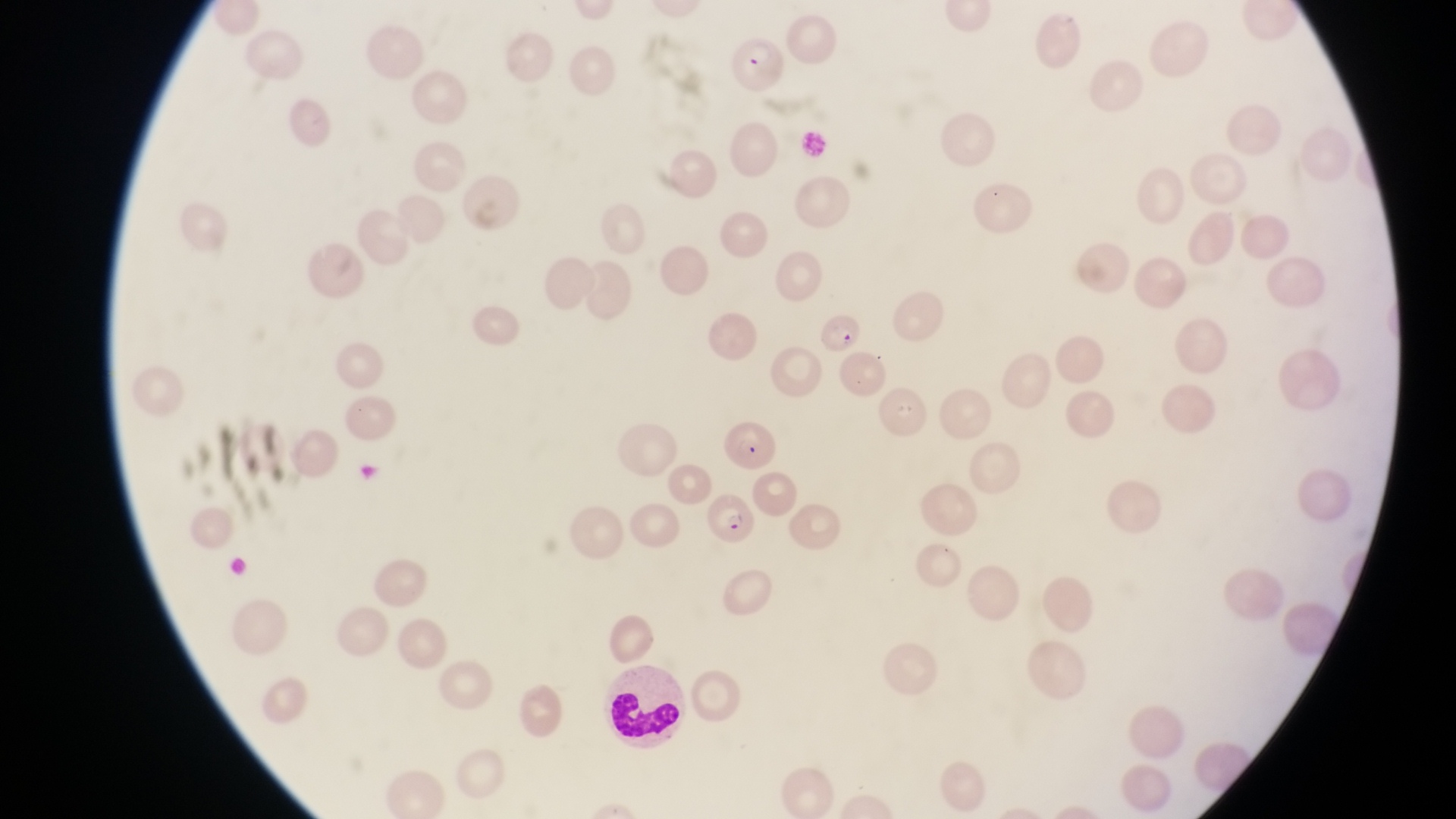

Approximate bounding boxes as left top right bottom in pixels. Parasitised red blood cell locations: 726 33 793 100; 816 307 861 350; 720 410 775 470; 706 494 759 553. Object labeled both leukocyte and parasitised red blood cell by the source: 601 655 693 750. Photographed through the eyepiece of an Olympus CX-23 microscope with a smartphone camera. Thin blood smear. Magnification of 1000x. Collected in Uganda. Single field of view. Image is 1456×819 pixels.